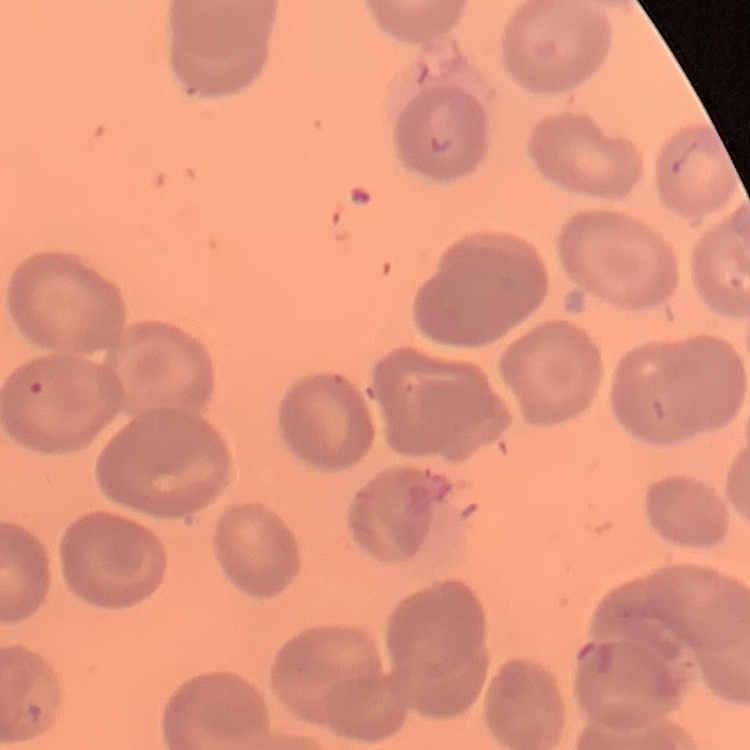

erythrocyte_morphology: no rouleaux formation
image_type: one tile cut from a larger photomicrograph
stain: Field's or Giemsa
preparation: thin blood smear